Mark where cells are.
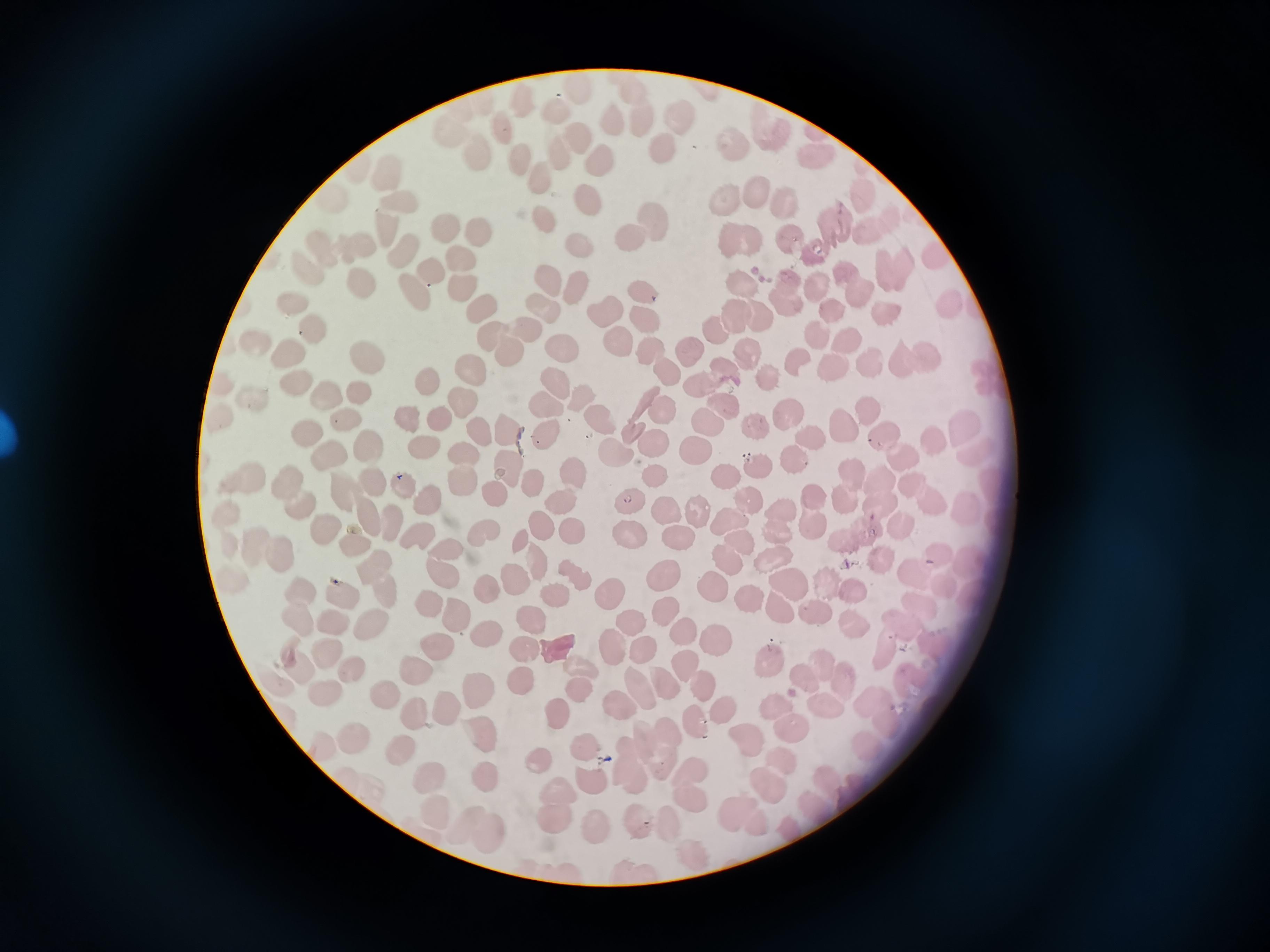

Approximate centers as {x, y} in pixels.
Cells: {678, 116}, {612, 120}, {504, 129}, {579, 141}, {734, 141}, {664, 149}, {558, 154}, {479, 156}, {821, 157}, {520, 158}, {608, 161}, {388, 171}, {539, 178}, {758, 195}, {585, 197}, {399, 198}, {727, 200}, {788, 201}, {543, 217}, {655, 219}, {388, 226}, {836, 227}, {447, 229}, {480, 233}, {742, 235}, {631, 236}, {791, 236}, {578, 243}, {331, 248}, {406, 252}, {818, 252}, {464, 260}, {306, 267}, {895, 271}, {435, 272}, {846, 273}, {362, 279}, {551, 280}, {743, 282}, {463, 286}, {576, 286}, {817, 289}, {416, 290}, {646, 291}, {786, 293}, {860, 297}, {290, 299}, {952, 305}, {549, 308}, {607, 308}, {482, 312}, {736, 315}, {887, 315}, {648, 317}, {762, 317}, {715, 328}, {310, 329}, {526, 329}, {820, 332}, {493, 337}, {847, 340}, {617, 341}, {565, 345}, {650, 349}, {688, 349}, {510, 351}, {290, 352}, {750, 354}, {370, 356}, {800, 362}, {919, 362}, {833, 367}, {472, 368}, {873, 368}, {666, 372}, {728, 374}, {771, 378}, {428, 381}, {555, 382}, {295, 383}, {360, 390}, {697, 390}, {256, 394}, {323, 395}, {583, 397}, {465, 402}, {545, 403}, {726, 403}, {661, 409}, {868, 411}, {787, 414}, {348, 418}, {409, 418}, {442, 418}, {605, 420}, {710, 424}, {758, 424}, {844, 425}, {966, 428}, {477, 430}, {508, 434}, {549, 435}, {306, 436}, {883, 438}, {812, 440}, {936, 440}, {656, 444}, {423, 445}, {698, 447}, {371, 448}, {328, 450}, {615, 450}, {466, 455}, {796, 460}, {907, 461}, {760, 466}, {512, 468}, {577, 470}, {850, 473}, {656, 474}, {727, 475}, {375, 477}, {245, 478}, {462, 480}, {535, 481}, {885, 481}, {402, 486}, {301, 491}, {345, 494}, {495, 494}, {748, 496}, {925, 497}, {565, 500}, {631, 502}, {845, 502}, {433, 503}, {665, 507}, {699, 510}, {813, 511}, {968, 511}, {378, 520}, {732, 524}, {781, 525}, {546, 528}, {864, 528}, {329, 530}, {904, 531}, {573, 532}, {631, 534}, {419, 536}, {485, 536}, {679, 537}, {523, 542}, {362, 545}, {271, 549}, {450, 550}, {774, 559}, {887, 561}, {539, 563}, {729, 563}, {447, 571}, {667, 576}, {918, 576}, {520, 579}, {382, 580}, {792, 581}, {718, 587}, {844, 587}, {489, 590}, {345, 594}, {560, 594}, {611, 595}, {750, 596}, {431, 605}, {782, 610}, {668, 611}, {813, 611}, {461, 616}, {537, 617}, {634, 619}, {852, 621}, {332, 622}, {374, 628}, {486, 630}, {683, 632}, {715, 641}, {615, 647}, {645, 647}, {442, 648}, {325, 650}, {526, 650}, {769, 660}, {580, 665}, {418, 668}, {295, 669}, {356, 673}, {523, 676}, {693, 677}, {821, 677}, {664, 679}, {645, 689}, {480, 690}, {580, 691}, {329, 693}, {385, 693}, {619, 705}, {829, 705}, {446, 709}, {728, 710}, {417, 715}, {559, 716}, {790, 721}, {698, 722}, {356, 735}, {484, 736}, {747, 739}, {586, 745}, {660, 747}, {399, 749}, {540, 758}, {631, 766}, {429, 777}, {490, 778}, {768, 779}, {590, 781}, {694, 785}, {439, 808}, {554, 808}, {744, 813}, {637, 818}, {669, 823}, {595, 825}, {477, 828}.

stain: Giemsa
image_size: 1270×952 pixels
capture: smartphone through the microscope eyepiece
preparation: thin smear
field_of_view: single